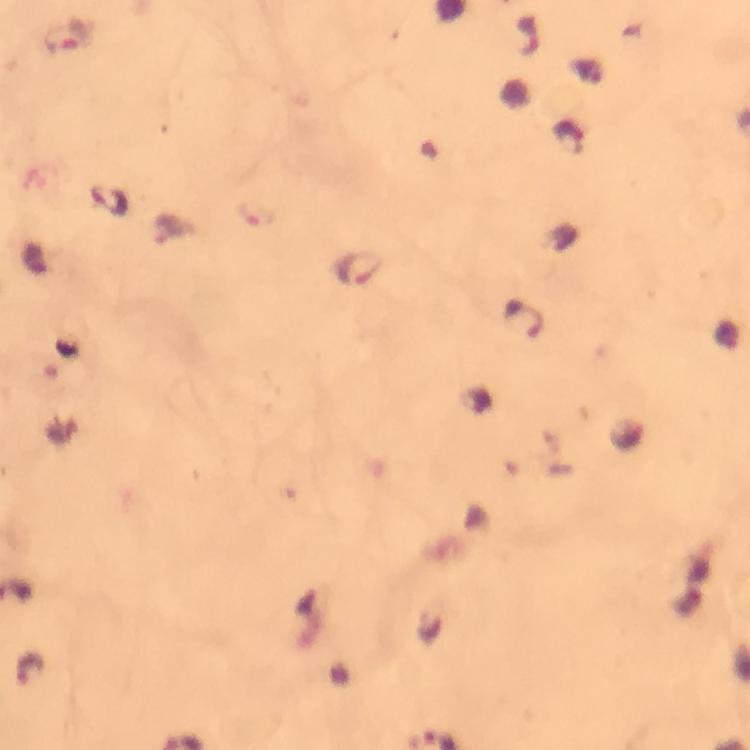
Approximate object centers, in pixels from the top-left corner.
Summary:
  - Plasmodium parasite locations: (x=67, y=36), (x=110, y=199), (x=170, y=229), (x=357, y=267), (x=521, y=317)
  - Stain: Giemsa
  - Magnification: 100x
  - Image size: 750×750 pixels
  - Cropped from: one field of view
  - Immersion oil: applied
  - Capture: smartphone mounted on the microscope
  - Preparation: thick blood film
  - Context: from a malaria diagnostic workup